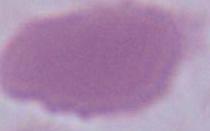

{
  "magnification": "1000x",
  "identification": "erythrocyte",
  "modality": "micrograph"
}